Locate every leukocyte (white blood cell).
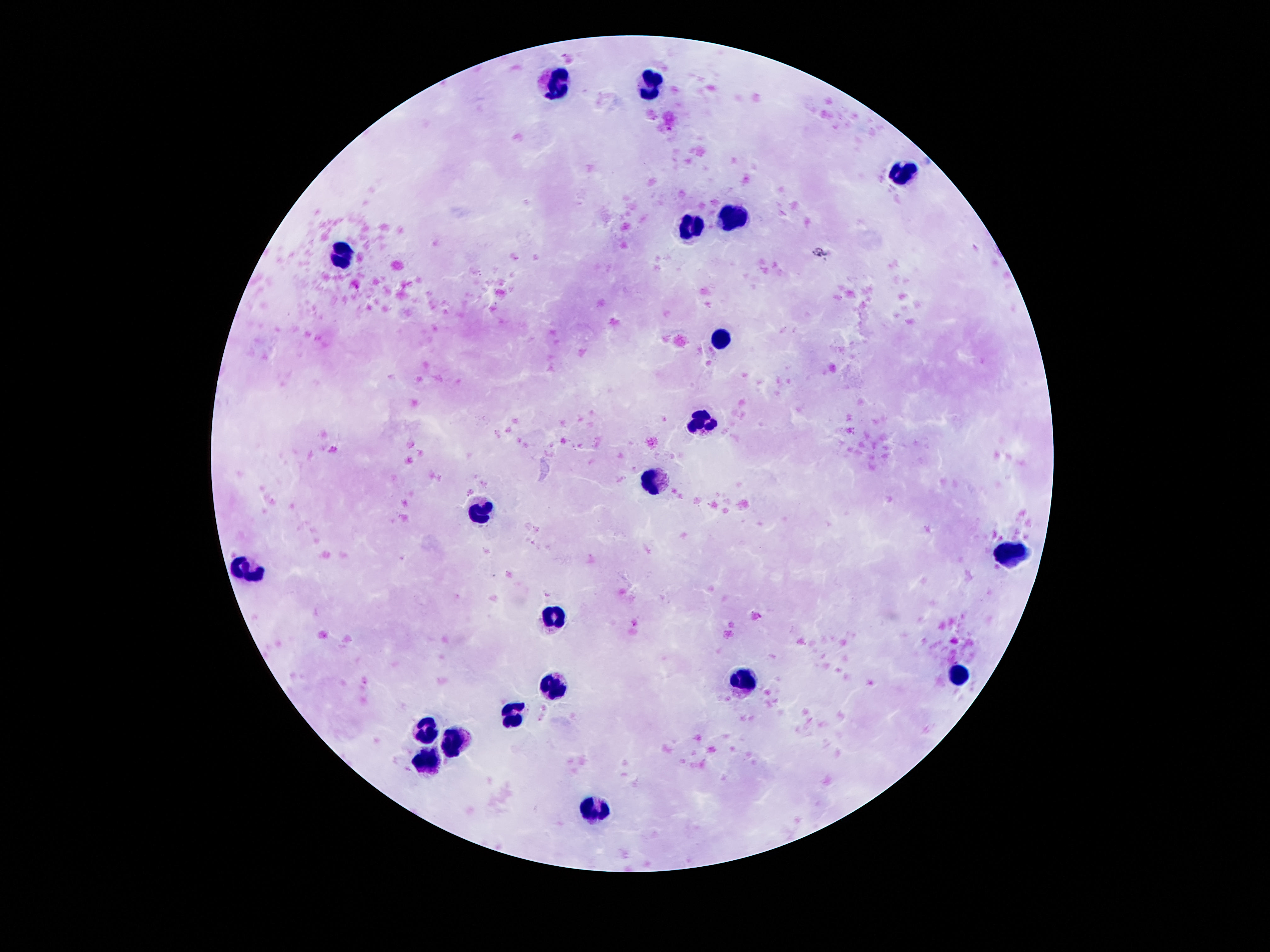
Approximate centers as [x, y] in pixels.
Leukocytes: [556, 82], [653, 85], [908, 173], [735, 219], [694, 227], [342, 257], [722, 340], [706, 420], [656, 481], [483, 514], [1010, 550], [252, 574], [556, 618], [962, 675], [747, 681], [556, 685], [518, 714], [429, 730], [456, 741], [427, 760], [595, 810].

stain: Giemsa
field_of_view: single
capture: smartphone camera through the microscope eyepiece
image_size: 1270×952 pixels
preparation: thick peripheral-blood smear
patient_malaria_status: uninfected
magnification: 100x